Identify the parasite.
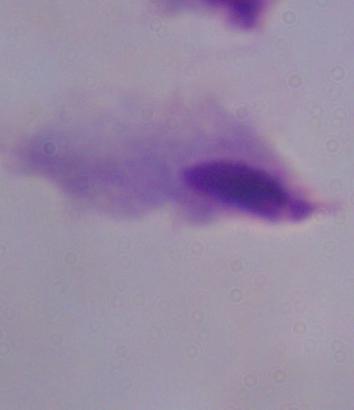
This is a trichomonad.

Photomicrograph. Captured at 1000x magnification.